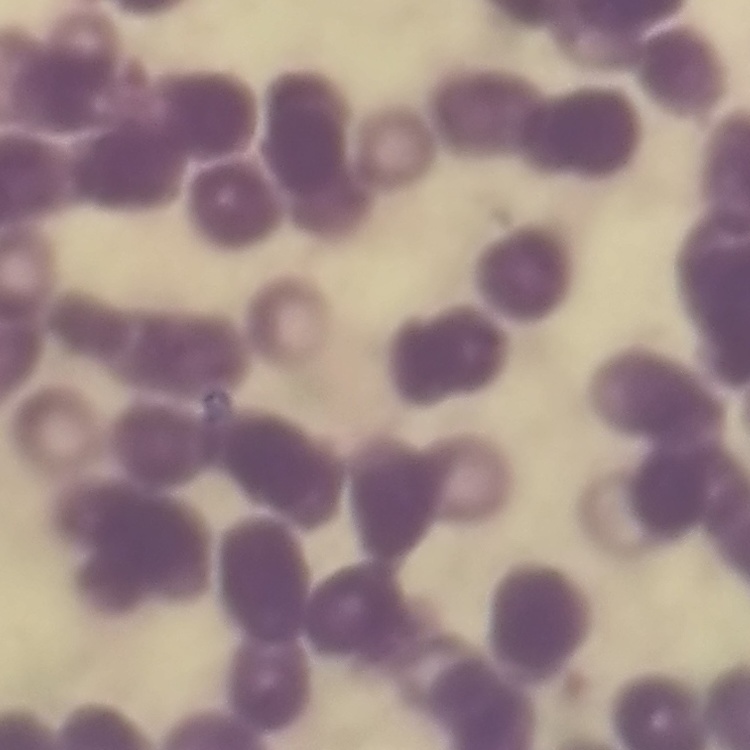
The erythrocytes show rouleaux formation. Stained with either Field's or Giemsa. Thin peripheral smear. Square crop of a larger photomicrograph.